State which parasite is depicted.
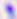

This is Toxoplasma gondii.

400x magnification. Photomicrograph.